Assess the morphology of the red blood cells.
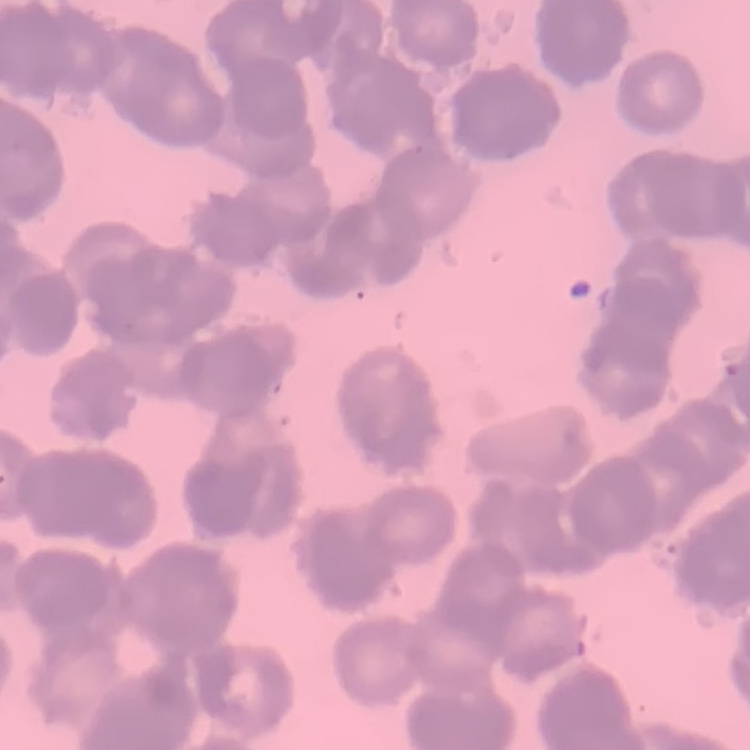

Rouleaux formation.

Summary:
  - Preparation: thin blood smear
  - Image type: square crop of a larger photomicrograph
  - Stain: Field's or Giemsa